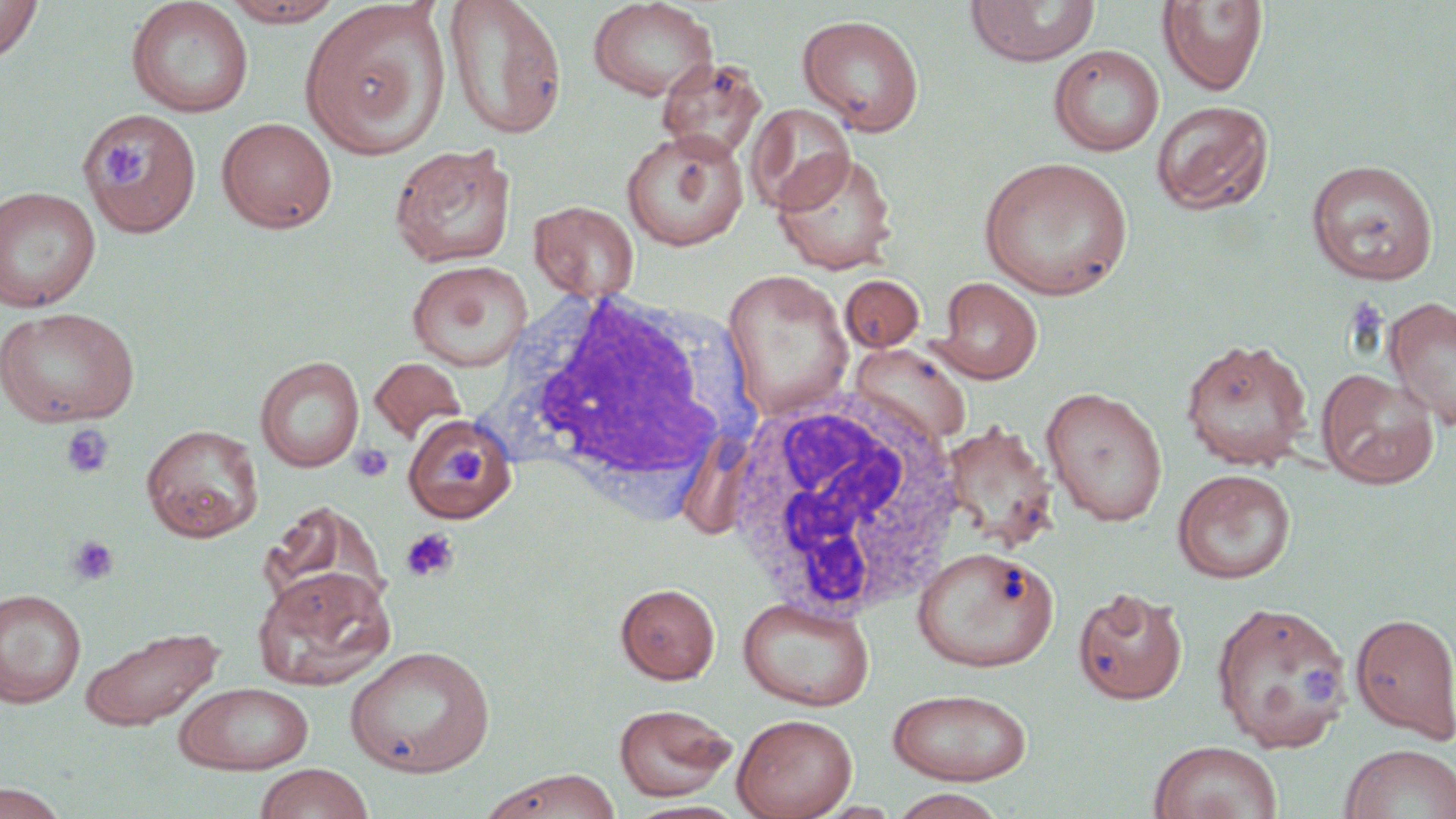

Summary:
  - Coordinate format: approximate bounding boxes as (x1,y1)-(x2,y2) corner pairs in pixels
  - White blood cell locations: (485,283)-(762,524), (724,386)-(967,623)
  - Uninfected red blood cell locations: (0,0)-(43,63), (218,0)-(347,27), (441,0)-(568,141), (587,0)-(720,102), (126,1)-(254,118), (298,1)-(452,159), (966,1)-(1101,67), (1157,1)-(1269,96), (797,14)-(925,136), (1049,44)-(1164,157), (656,57)-(769,162), (1151,100)-(1275,215), (746,102)-(856,214), (84,107)-(201,239), (216,117)-(337,234), (620,128)-(749,251), (389,142)-(516,269), (773,150)-(898,275), (978,156)-(1134,301), (1305,159)-(1439,285), (0,185)-(102,312), (529,200)-(639,302), (407,259)-(533,371), (721,268)-(854,420), (840,274)-(925,352), (935,276)-(1043,384), (1384,297)-(1456,431), (0,306)-(140,428), (1180,338)-(1313,469), (848,342)-(972,445), (255,356)-(364,473), (369,357)-(467,444), (1316,368)-(1439,488), (1041,387)-(1168,526), (402,415)-(517,524), (141,424)-(264,542), (1172,468)-(1296,584), (260,503)-(389,619), (913,546)-(1058,671), (251,565)-(396,691), (616,582)-(721,683), (1073,586)-(1188,705), (0,588)-(87,708), (738,595)-(875,711), (1210,600)-(1351,753), (1350,612)-(1456,744), (77,623)-(226,732), (344,645)-(495,777), (173,681)-(314,774), (888,688)-(1033,785), (614,703)-(737,801), (732,713)-(857,819), (1148,741)-(1283,819), (1339,743)-(1456,819), (253,763)-(376,819), (479,768)-(623,819), (0,783)-(73,819), (889,789)-(1009,819)
  - Platelet locations: (99,141)-(140,185), (60,423)-(115,480), (438,442)-(488,497), (349,443)-(394,483), (400,527)-(460,583), (66,535)-(119,586), (1302,664)-(1344,704)
  - Slide-level diagnosis: negative for blood parasites
  - Field of view: single
  - Magnification: 1000x
  - Modality: light microscopy
  - Preparation: thin blood film
  - Stain: May-Grünwald-Giemsa
  - Image size: 1456×819 pixels